State which cell type is depicted.
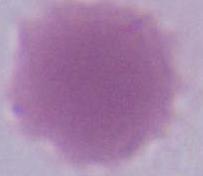

This is an erythrocyte.

Summary:
  - Magnification: 1000x
  - Modality: photomicrograph